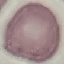 Result: negative for malaria parasites. Acquired by smartphone through the microscope eyepiece. Giemsa stain. Cell patch, automatically extracted from a larger field of view and resized to 64 × 64 pixels. Thin smear of blood.